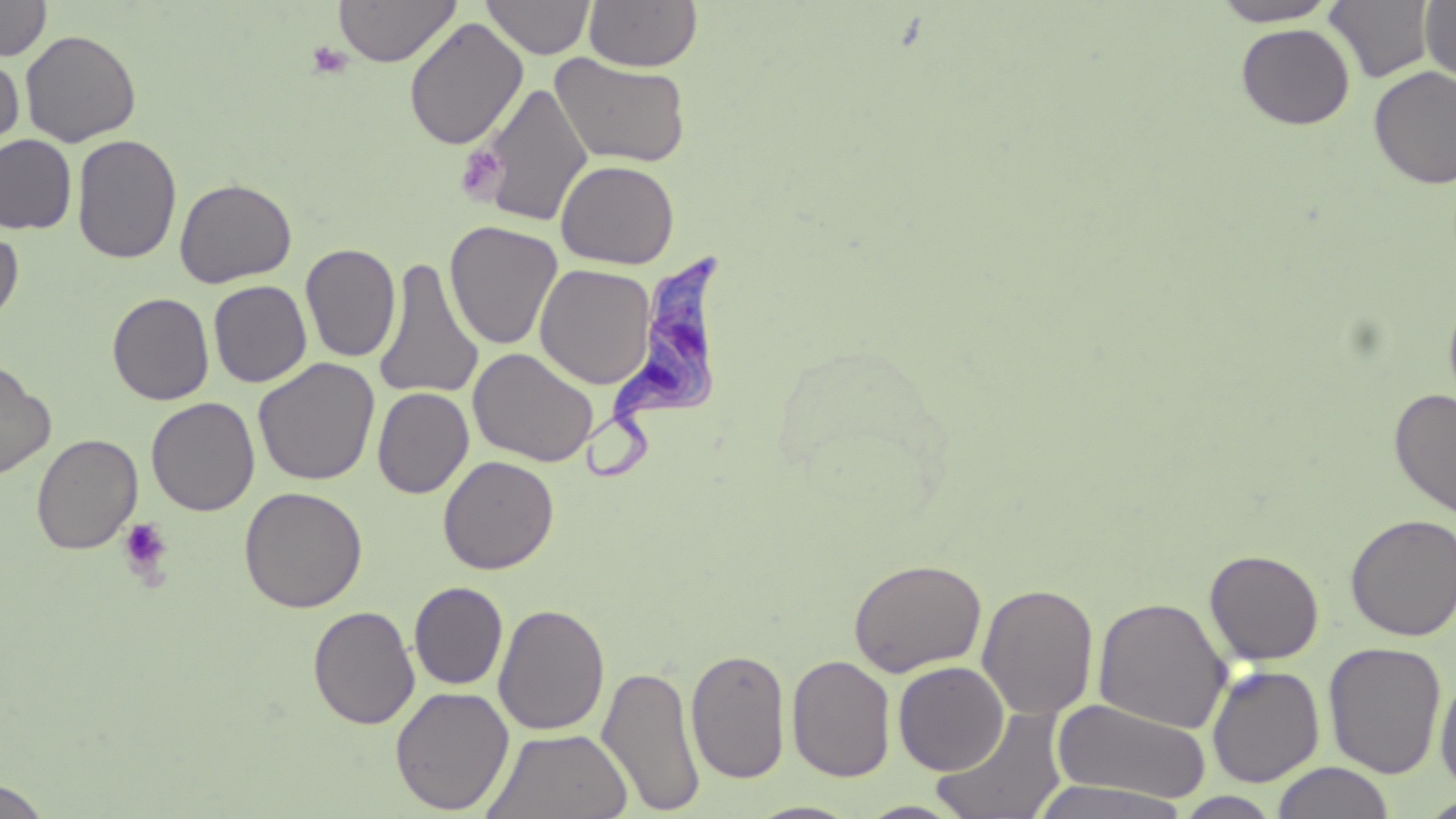

{
  "slide_level_diagnosis": "Trypanosoma brucei",
  "platelet_locations": "approximate bounding boxes as named x1/y1/x2/y2 corners in pixels: (x1=306, y1=41, x2=352, y2=80), (x1=456, y1=145, x2=506, y2=202), (x1=118, y1=518, x2=173, y2=582)",
  "stain": "May-Grünwald-Giemsa",
  "trypanosoma_brucei_locations": "approximate bounding boxes as named x1/y1/x2/y2 corners in pixels: (x1=578, y1=252, x2=735, y2=485)",
  "magnification": "1000x",
  "modality": "optical microscopy",
  "field_of_view": "one of a larger specimen",
  "uninfected_red_blood_cell_locations": "approximate bounding boxes as named x1/y1/x2/y2 corners in pixels: (x1=0, y1=0, x2=51, y2=60), (x1=333, y1=0, x2=460, y2=67), (x1=482, y1=0, x2=595, y2=59), (x1=1209, y1=0, x2=1342, y2=26), (x1=583, y1=1, x2=702, y2=72), (x1=1325, y1=1, x2=1436, y2=83), (x1=1420, y1=1, x2=1456, y2=85), (x1=404, y1=16, x2=528, y2=151), (x1=1236, y1=23, x2=1355, y2=129), (x1=20, y1=29, x2=141, y2=147), (x1=550, y1=53, x2=692, y2=168), (x1=0, y1=54, x2=24, y2=159), (x1=1368, y1=66, x2=1456, y2=190), (x1=478, y1=82, x2=593, y2=228), (x1=72, y1=133, x2=182, y2=265), (x1=0, y1=134, x2=77, y2=235), (x1=555, y1=159, x2=680, y2=269), (x1=174, y1=178, x2=297, y2=288), (x1=445, y1=220, x2=562, y2=350), (x1=0, y1=227, x2=24, y2=330), (x1=300, y1=243, x2=401, y2=363), (x1=374, y1=257, x2=484, y2=402), (x1=537, y1=263, x2=658, y2=390), (x1=208, y1=280, x2=312, y2=387), (x1=107, y1=292, x2=214, y2=405), (x1=468, y1=347, x2=599, y2=467), (x1=253, y1=357, x2=380, y2=486), (x1=0, y1=361, x2=56, y2=480), (x1=372, y1=386, x2=474, y2=498), (x1=1389, y1=387, x2=1456, y2=521), (x1=146, y1=396, x2=260, y2=516), (x1=31, y1=434, x2=142, y2=554), (x1=438, y1=455, x2=559, y2=574), (x1=238, y1=486, x2=368, y2=613), (x1=1345, y1=513, x2=1456, y2=642), (x1=1204, y1=548, x2=1325, y2=665), (x1=847, y1=558, x2=987, y2=677), (x1=409, y1=581, x2=508, y2=690), (x1=977, y1=582, x2=1099, y2=720), (x1=1092, y1=596, x2=1232, y2=735), (x1=493, y1=603, x2=610, y2=736), (x1=308, y1=605, x2=420, y2=729), (x1=1323, y1=641, x2=1447, y2=779), (x1=686, y1=648, x2=791, y2=785), (x1=786, y1=654, x2=896, y2=782), (x1=893, y1=661, x2=1009, y2=775), (x1=597, y1=663, x2=705, y2=816), (x1=1206, y1=665, x2=1325, y2=787), (x1=1435, y1=671, x2=1456, y2=796), (x1=390, y1=685, x2=514, y2=814), (x1=1052, y1=698, x2=1209, y2=803), (x1=930, y1=705, x2=1069, y2=818), (x1=482, y1=727, x2=633, y2=819), (x1=1271, y1=762, x2=1396, y2=819), (x1=0, y1=778, x2=51, y2=818), (x1=1028, y1=780, x2=1192, y2=819), (x1=1175, y1=792, x2=1283, y2=818), (x1=1417, y1=795, x2=1456, y2=818), (x1=856, y1=800, x2=968, y2=818), (x1=746, y1=801, x2=863, y2=819)",
  "preparation": "thin blood smear",
  "image_size": "1456×819 pixels"
}